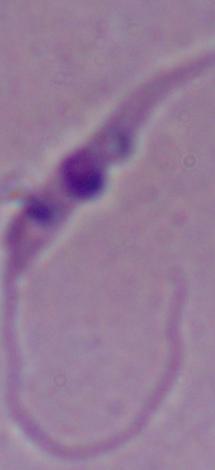 A Leishmania parasite is seen. Micrograph. 1000x magnification.